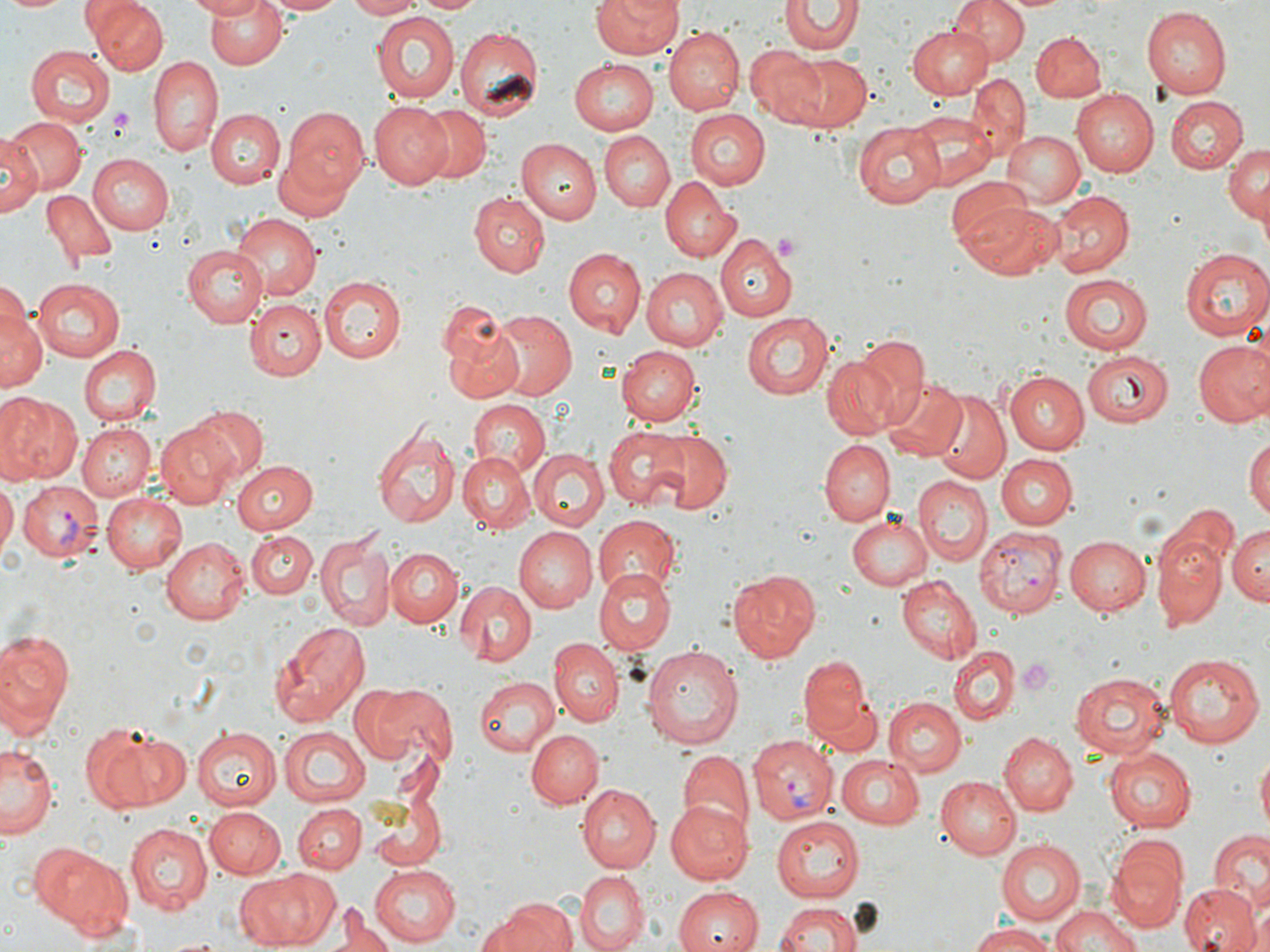
Approximate bounding boxes as (x1,y1)-(x2,y2) corner pairs in pixels. Plasmodium vivax-infected red blood cell locations: (17,484)-(102,564), (975,527)-(1068,617), (749,741)-(832,822). Platelet locations: (109,108)-(135,139), (772,231)-(801,255), (1018,658)-(1057,696). Uninfected red blood cell locations: (1,0)-(74,15), (90,0)-(165,74), (187,0)-(266,20), (205,0)-(289,69), (261,0)-(347,15), (346,0)-(421,20), (412,0)-(485,16), (591,0)-(683,59), (948,0)-(1029,66), (780,2)-(861,57), (1139,8)-(1229,98), (372,12)-(459,103), (904,24)-(993,102), (455,26)-(545,121), (664,28)-(744,114), (1030,31)-(1106,103), (746,45)-(829,128), (26,46)-(114,125), (786,54)-(872,132), (148,56)-(224,158), (569,58)-(659,136), (967,72)-(1028,159), (1071,89)-(1159,177), (1166,95)-(1249,173), (368,101)-(453,190), (411,103)-(492,183), (682,108)-(768,191), (207,109)-(284,189), (282,111)-(369,197), (910,112)-(997,189), (5,114)-(85,195), (853,122)-(944,208), (600,131)-(674,211), (1002,131)-(1085,209), (0,135)-(42,216), (518,136)-(602,225), (270,138)-(361,219), (1223,143)-(1269,226), (88,154)-(174,234), (660,177)-(740,262), (948,178)-(1034,257), (42,187)-(116,266), (1048,188)-(1131,276), (1052,191)-(1139,355), (470,193)-(549,276), (963,200)-(1061,279), (230,212)-(321,300), (716,235)-(798,322), (183,246)-(269,328), (562,247)-(644,336), (1180,248)-(1269,339), (640,267)-(727,352), (317,275)-(405,364), (1058,275)-(1154,356), (33,278)-(123,360), (4,280)-(84,383), (1,295)-(44,399), (248,299)-(326,380), (487,311)-(577,402), (742,311)-(835,400), (441,313)-(526,406), (854,334)-(933,429), (1192,339)-(1270,426), (77,345)-(161,426), (617,345)-(700,426), (1080,350)-(1172,428), (823,357)-(899,442), (1004,368)-(1092,455), (883,379)-(966,461), (932,392)-(1009,484), (0,393)-(79,484), (468,400)-(549,477), (185,404)-(269,484), (155,420)-(240,509), (77,423)-(156,500), (372,424)-(460,530), (603,426)-(693,510), (648,429)-(732,515), (1246,437)-(1270,527), (820,440)-(895,526), (529,449)-(608,530), (459,450)-(536,531), (997,454)-(1077,529), (231,461)-(318,535), (915,475)-(991,562), (0,480)-(17,560), (104,491)-(189,574), (1159,499)-(1239,582), (848,513)-(934,590), (593,515)-(681,597), (1227,525)-(1269,609), (514,528)-(596,613), (246,529)-(317,602), (315,530)-(396,631), (1153,533)-(1227,629), (1063,535)-(1152,616), (163,537)-(250,625), (384,547)-(462,626), (591,566)-(674,654), (726,568)-(819,663), (896,576)-(983,663), (456,581)-(537,665), (267,620)-(371,727), (0,629)-(75,733), (549,638)-(622,727), (642,643)-(744,750), (948,648)-(1017,725), (1163,651)-(1264,746), (797,654)-(874,742), (1069,669)-(1171,757), (472,676)-(559,757), (357,681)-(452,767), (885,697)-(966,777), (867,699)-(982,830), (83,725)-(188,812), (190,727)-(278,811), (278,728)-(371,807), (526,729)-(603,806), (999,732)-(1077,815), (1,744)-(59,841), (1104,746)-(1198,832), (675,749)-(754,837), (1256,753)-(1270,833), (836,755)-(927,831), (935,775)-(1020,860), (578,784)-(660,872), (364,789)-(448,874), (665,799)-(751,884), (292,803)-(365,875), (204,806)-(286,880), (771,815)-(864,899), (124,823)-(212,914), (1210,829)-(1270,903), (995,839)-(1085,927), (1107,841)-(1187,930), (27,845)-(133,935), (371,866)-(460,947), (239,868)-(341,949), (575,871)-(648,951), (1252,881)-(1270,950), (1181,885)-(1258,952), (673,886)-(763,952), (488,896)-(575,952), (773,900)-(859,952), (335,905)-(386,952), (1052,906)-(1143,952), (967,922)-(1058,951). Slide-level diagnosis: Plasmodium vivax. May-Grünwald-Giemsa stain. Thin blood smear. 1000x magnification. Image is 1270×952 pixels. Light microscopy. Single field of view.